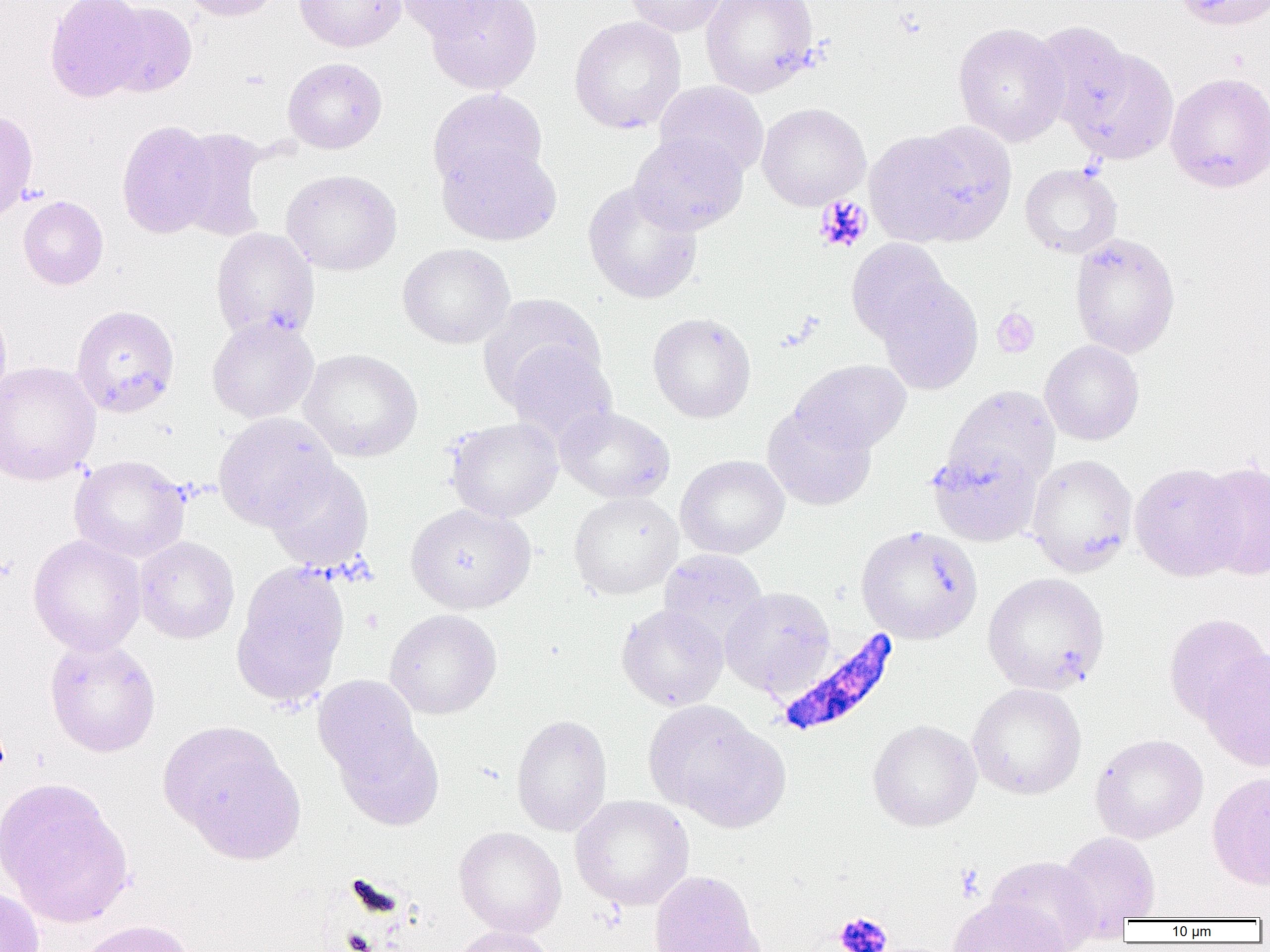

Approximate bounding boxes as (x1,y1)-(x2,y2) corner pairs in pixels. Platelet locations: (814,194)-(873,253), (992,308)-(1040,358), (833,912)-(892,952). Uninfected red blood cell locations: (44,0)-(151,102), (179,0)-(282,21), (294,0)-(406,52), (394,0)-(511,42), (624,0)-(729,37), (701,0)-(819,97), (1175,0)-(1270,31), (425,1)-(542,95), (103,2)-(197,96), (569,16)-(686,134), (1030,21)-(1135,132), (953,22)-(1070,145), (1063,45)-(1179,166), (282,57)-(387,154), (1165,72)-(1270,192), (654,81)-(770,181), (428,88)-(547,193), (756,103)-(870,210), (0,110)-(38,222), (117,119)-(220,239), (867,124)-(1015,247), (172,128)-(269,241), (629,131)-(748,236), (437,141)-(562,246), (1020,164)-(1123,259), (281,169)-(402,276), (582,182)-(703,304), (18,196)-(109,291), (210,228)-(319,340), (1069,232)-(1180,359), (846,238)-(951,343), (397,243)-(515,349), (875,276)-(983,394), (478,295)-(605,407), (0,298)-(12,407), (71,304)-(180,418), (647,312)-(756,423), (207,315)-(319,423), (1041,340)-(1144,445), (506,344)-(617,447), (298,348)-(422,462), (790,359)-(911,454), (0,361)-(101,485), (945,385)-(1060,490), (762,405)-(877,510), (555,406)-(675,503), (212,412)-(338,531), (445,417)-(564,522), (927,442)-(1042,546), (676,454)-(790,559), (1025,454)-(1137,576), (69,455)-(190,563), (264,460)-(374,573), (1196,461)-(1270,582), (1130,463)-(1245,581), (568,492)-(683,600), (406,503)-(535,614), (856,526)-(983,644), (28,535)-(147,656), (134,536)-(240,644), (658,550)-(768,648), (232,562)-(350,708), (982,572)-(1109,694), (720,587)-(835,696), (616,604)-(728,711), (384,609)-(502,719), (1163,612)-(1269,727), (44,637)-(161,757), (1200,648)-(1270,771), (313,675)-(422,783), (967,683)-(1087,800), (645,700)-(790,832), (511,715)-(613,836), (868,719)-(981,832), (161,722)-(302,860), (334,723)-(444,831), (1089,733)-(1208,843), (1207,772)-(1270,890), (0,778)-(135,928), (570,795)-(694,910), (454,826)-(566,938), (1056,831)-(1161,931), (986,855)-(1102,952), (648,870)-(763,952), (0,884)-(45,952), (947,897)-(1072,952), (75,919)-(200,952), (449,926)-(557,952). Plasmodium falciparum-infected red blood cell locations: (774,627)-(900,738). Slide-level diagnosis: Plasmodium falciparum. Thin blood film. Image is 1270×952 pixels. 1000x magnification. Optical microscopy. Single field of view.